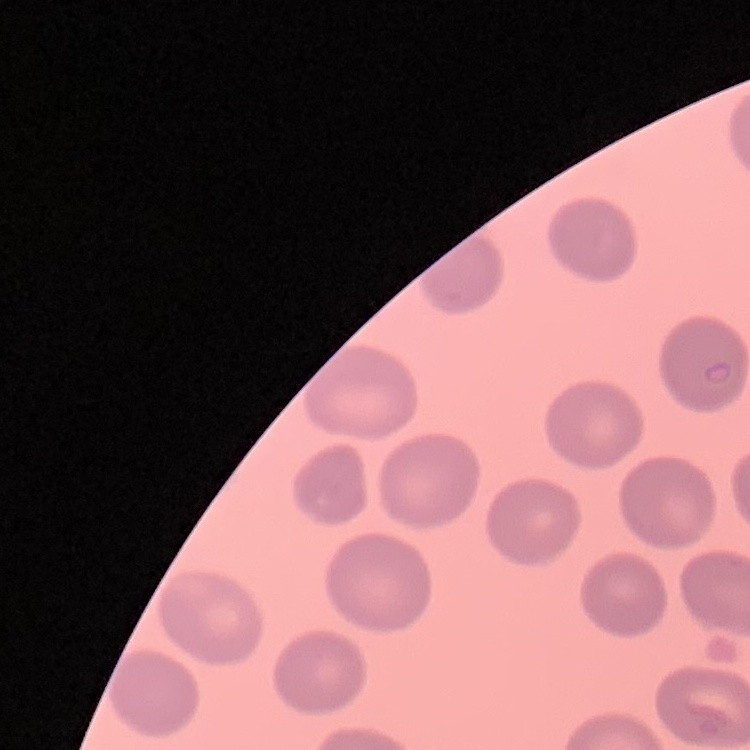
{
  "erythrocyte_morphology": "no rouleaux formation",
  "preparation": "thin peripheral smear",
  "stain": "Field's or Giemsa",
  "image_type": "one tile cut from a larger photomicrograph"
}